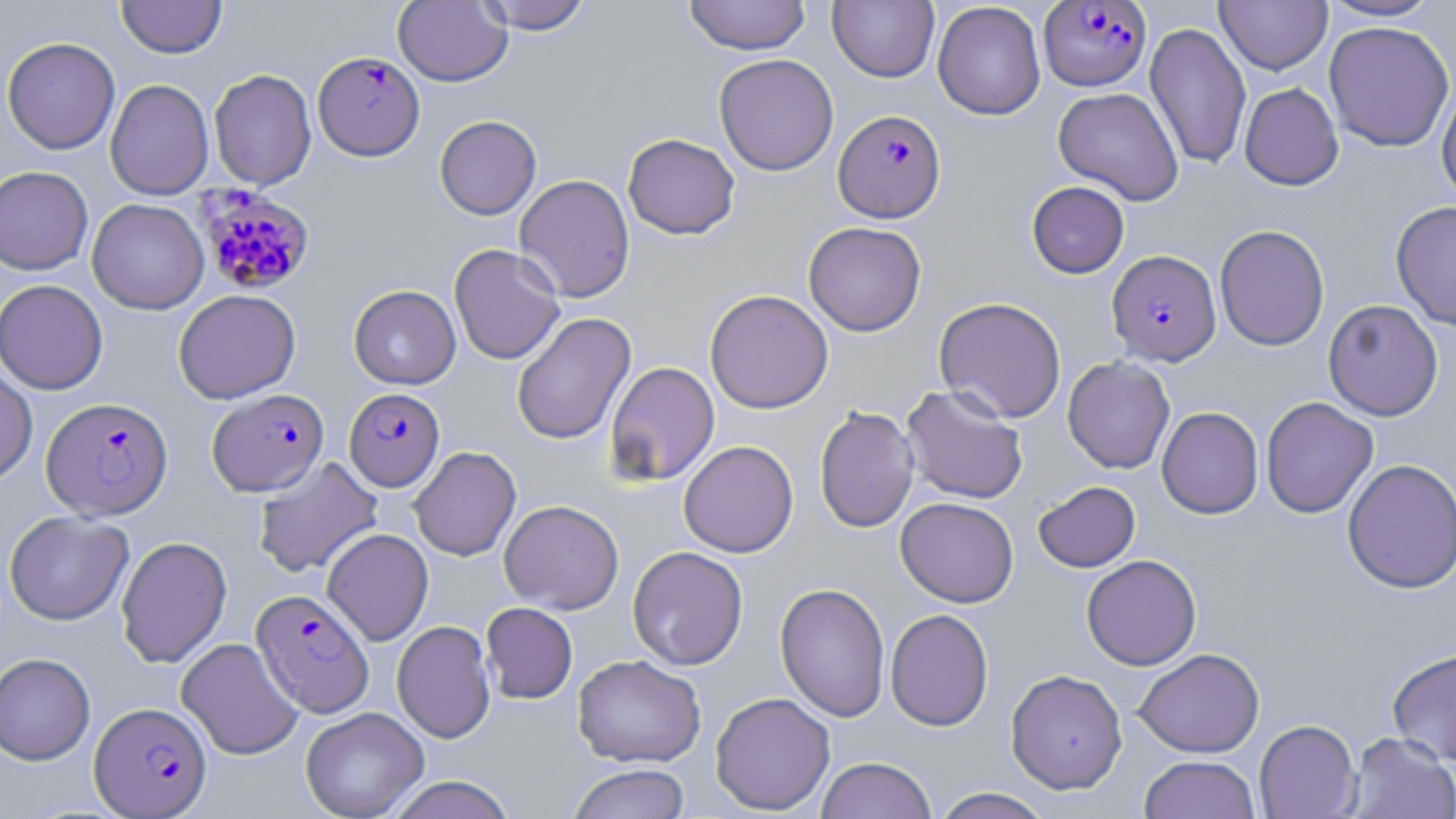

Summary:
  - Coordinate format: approximate bounding boxes as (x1, y1, x2, y2) in pixels
  - Plasmodium falciparum-infected red blood cell locations: (1039, 1, 1151, 91), (314, 51, 424, 160), (833, 109, 946, 223), (196, 187, 316, 296), (1106, 249, 1221, 366), (344, 387, 445, 491), (207, 388, 329, 497), (41, 396, 173, 520), (251, 589, 374, 717), (90, 701, 212, 817)
  - Uninfected red blood cell locations: (117, 0, 227, 59), (392, 0, 512, 87), (475, 0, 595, 34), (683, 0, 811, 56), (1318, 0, 1445, 21), (827, 1, 939, 83), (932, 1, 1046, 120), (1214, 1, 1332, 74), (1144, 21, 1251, 171), (1323, 21, 1455, 152), (2, 36, 121, 155), (714, 54, 839, 176), (209, 69, 316, 190), (105, 79, 213, 200), (1436, 81, 1456, 206), (1239, 82, 1344, 190), (1053, 87, 1184, 206), (434, 115, 542, 220), (623, 133, 740, 240), (0, 166, 93, 275), (514, 174, 635, 303), (1026, 181, 1130, 278), (87, 198, 209, 315), (1390, 201, 1456, 331), (803, 221, 926, 336), (1214, 224, 1330, 351), (449, 243, 565, 365), (0, 279, 109, 395), (348, 284, 461, 389), (173, 289, 301, 404), (704, 289, 834, 414), (933, 296, 1067, 423), (1323, 299, 1444, 421), (512, 312, 636, 445), (1062, 356, 1175, 473), (605, 361, 720, 485), (0, 362, 38, 487), (901, 384, 1029, 505), (1261, 396, 1379, 518), (814, 405, 919, 533), (1156, 406, 1263, 519), (678, 440, 799, 557), (409, 446, 521, 561), (253, 455, 383, 579), (1342, 458, 1456, 594), (1033, 481, 1140, 572), (895, 497, 1019, 608), (499, 500, 624, 614), (4, 511, 133, 625), (322, 528, 434, 646), (116, 535, 232, 668), (627, 546, 748, 670), (1081, 555, 1202, 670), (776, 582, 890, 722), (481, 602, 578, 704), (885, 608, 994, 732), (392, 620, 496, 743), (176, 638, 303, 760), (1387, 647, 1456, 765), (1133, 648, 1265, 758), (0, 653, 95, 765), (572, 654, 706, 768), (1006, 668, 1127, 794), (710, 692, 836, 815), (300, 706, 429, 819), (1254, 719, 1362, 818), (1346, 732, 1456, 818), (1139, 755, 1260, 819), (816, 756, 938, 819), (567, 763, 690, 819), (385, 775, 518, 819), (930, 787, 1055, 819)
  - Slide-level diagnosis: Plasmodium falciparum
  - Magnification: 1000x
  - Modality: optical microscopy
  - Stain: May-Grünwald-Giemsa
  - Field of view: single
  - Preparation: thin blood film
  - Image size: 1456×819 pixels